Identify the cell.
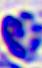

A leukocyte.

Summary:
  - Magnification: 400x
  - Modality: photomicrograph